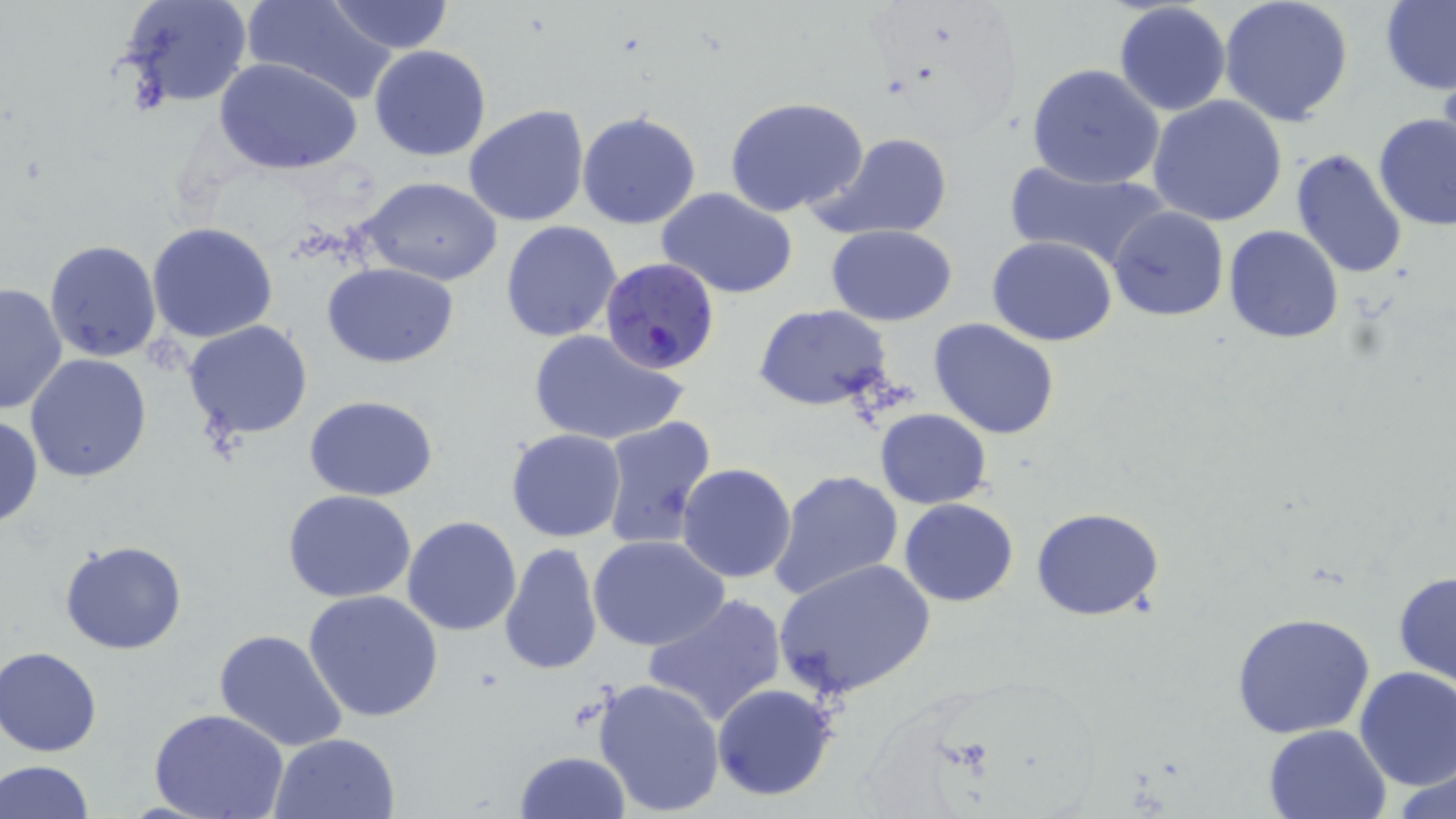 Approximate bounding boxes as [x1, y1, x2, y2] in pixels. Uninfected red blood cell locations: [117, 0, 254, 111], [244, 0, 393, 105], [326, 0, 456, 53], [1220, 0, 1354, 125], [1379, 0, 1456, 95], [1113, 1, 1233, 116], [369, 45, 492, 162], [215, 57, 364, 174], [1025, 63, 1167, 189], [1147, 93, 1288, 228], [723, 96, 870, 219], [463, 104, 590, 228], [577, 110, 702, 230], [1373, 113, 1456, 230], [817, 132, 953, 240], [1291, 148, 1409, 282], [1001, 161, 1173, 271], [357, 176, 502, 285], [655, 186, 799, 300], [1106, 205, 1230, 322], [500, 220, 622, 343], [146, 222, 279, 344], [827, 225, 958, 325], [1224, 226, 1345, 344], [987, 236, 1117, 346], [43, 240, 162, 363], [322, 263, 460, 366], [1, 281, 66, 416], [754, 304, 893, 412], [928, 317, 1061, 441], [182, 320, 315, 441], [526, 328, 689, 448], [25, 353, 152, 483], [305, 395, 440, 501], [874, 408, 992, 510], [0, 415, 43, 527], [598, 416, 717, 548], [505, 428, 626, 541], [677, 463, 798, 584], [769, 469, 905, 601], [283, 489, 418, 603], [898, 498, 1019, 605], [1030, 506, 1167, 621], [403, 516, 523, 637], [588, 535, 732, 654], [59, 538, 189, 655], [499, 542, 603, 676], [774, 557, 935, 700], [1394, 571, 1456, 689], [303, 589, 444, 723], [643, 594, 787, 729], [1231, 611, 1376, 740], [213, 628, 348, 752], [0, 646, 103, 756], [1353, 665, 1456, 789], [592, 676, 727, 816], [712, 682, 839, 802], [149, 709, 291, 819], [1263, 723, 1392, 818], [269, 732, 401, 818], [515, 750, 629, 819], [1, 759, 94, 818], [1393, 767, 1456, 818]. Plasmodium falciparum-infected red blood cell locations: [600, 257, 721, 377]. Slide-level diagnosis: Plasmodium falciparum. Single field of view. Thin blood smear. May-Grünwald-Giemsa-stained preparation. Captured at 1000x magnification. Image is 1456×819 pixels. Light microscopy.